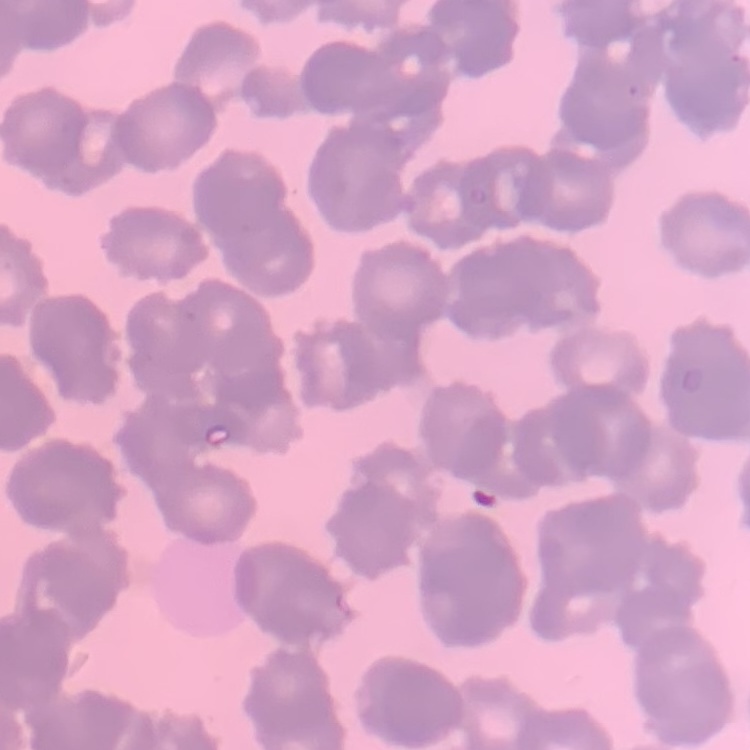

red blood cell morphology = rouleaux formation
stain = Field's or Giemsa
image type = square crop of a larger photomicrograph
preparation = thin peripheral smear